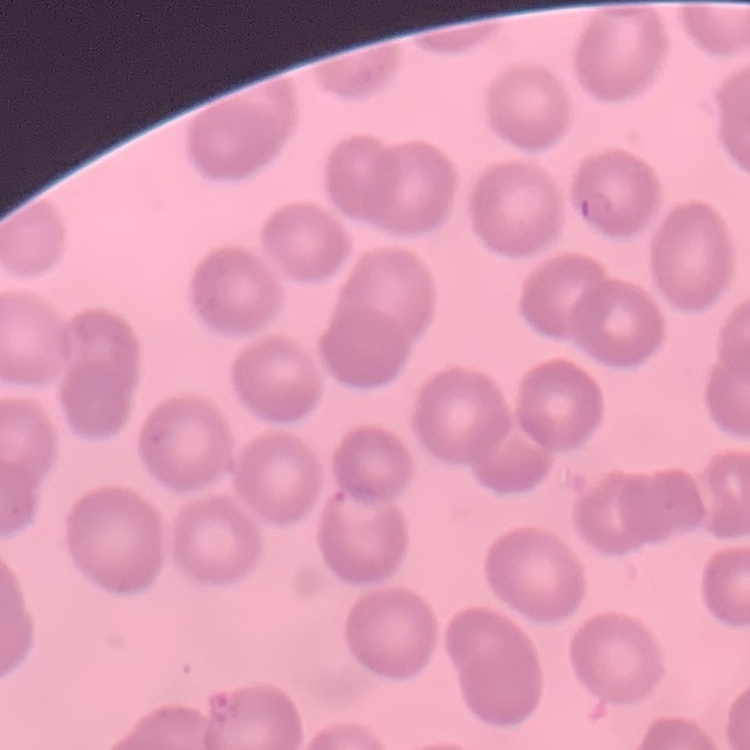
Summary:
  - Erythrocyte morphology: no rouleaux formation
  - Preparation: thin peripheral smear
  - Image type: square crop of a larger photomicrograph
  - Stain: Field's or Giemsa